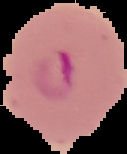
result = Plasmodium parasites detected
image size = 127×154 pixels
preparation = thin blood film
image type = cell region segmented out of the field of view; surrounding area masked to black